Comment on the morphology of the erythrocytes.
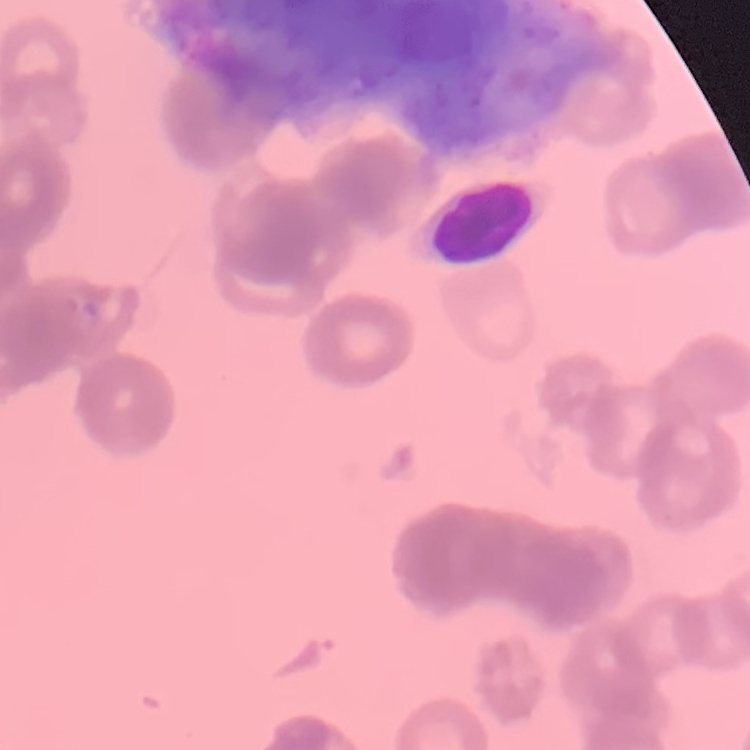
They show rouleaux formation.

Stained with either Field's or Giemsa. Square crop of a larger photomicrograph. Thin peripheral smear.